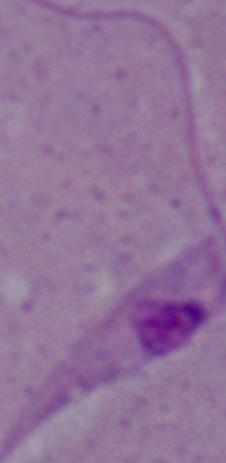

Summary:
  - Identification: Leishmania
  - Modality: photomicrograph
  - Magnification: 1000x